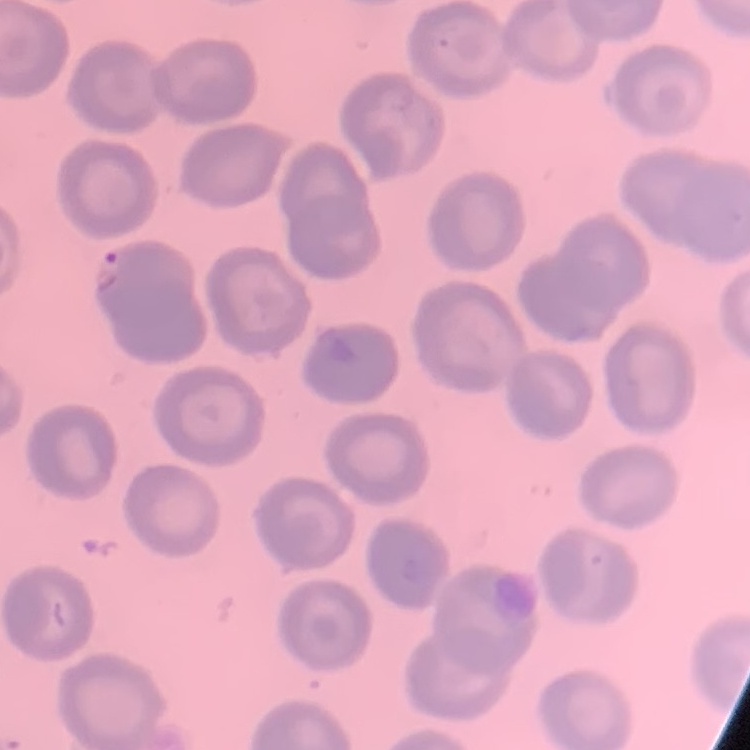
{
  "erythrocyte_morphology": "no rouleaux formation",
  "preparation": "thin blood smear",
  "image_type": "one tile cut from a larger photomicrograph",
  "stain": "Field's or Giemsa"
}